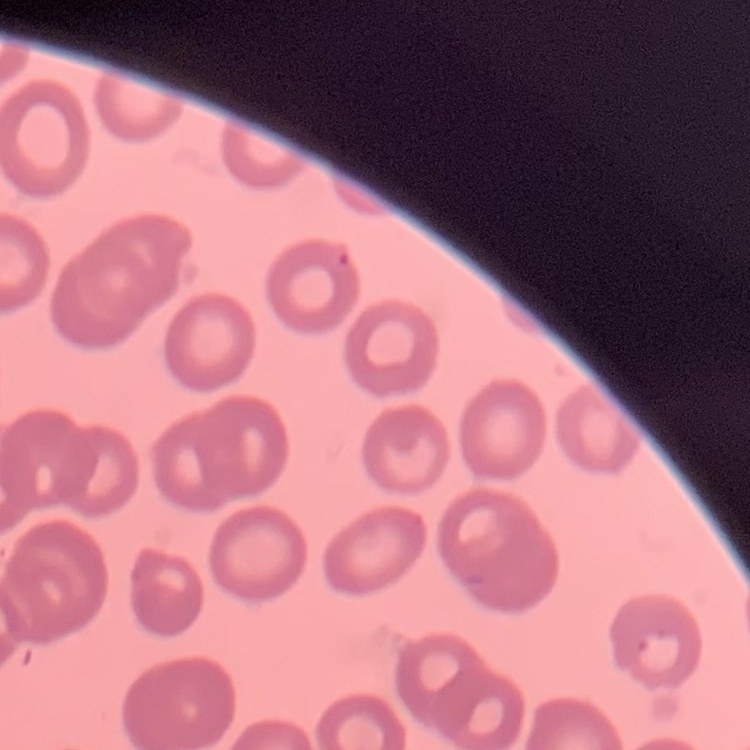
Summary:
  - Red blood cell morphology: no rouleaux formation
  - Image type: one tile cut from a larger photomicrograph
  - Preparation: thin blood smear
  - Stain: Field's or Giemsa